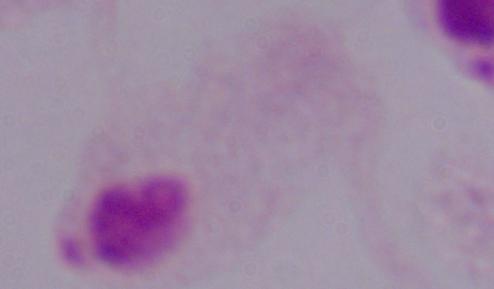

magnification: 1000x
identification: trichomonad
modality: photomicrograph